Report the malaria status of this cell.
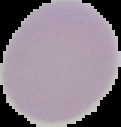
Uninfected.

image size = 121×127 pixels
preparation = thin blood film
image type = segmented cell region on a black background